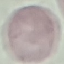
Malaria status: uninfected. Giemsa-stained preparation. Photographed with a smartphone camera at the microscope eyepiece. Cell patch, automatically extracted from a larger field of view and resized to 64 × 64 pixels. Thin blood smear.